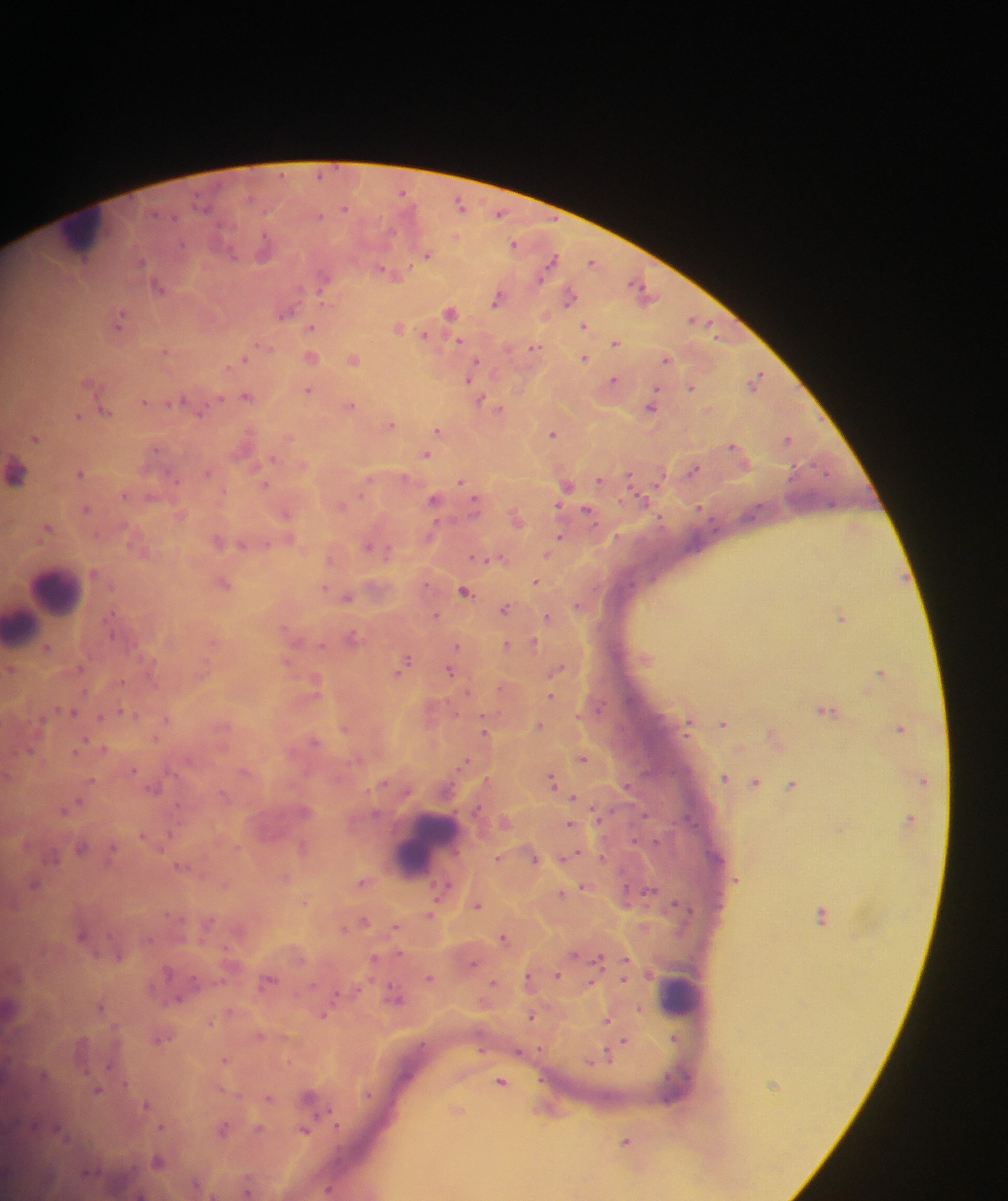 Approximate centers as {x, y} in pixels. Leukocyte locations: {83, 234}, {55, 592}, {20, 626}, {428, 842}, {680, 993}. Plasmodium parasite locations: {402, 192}, {203, 204}, {459, 204}, {344, 208}, {497, 214}, {318, 215}, {180, 244}, {513, 244}, {263, 247}, {427, 255}, {232, 256}, {140, 261}, {549, 261}, {591, 261}, {382, 270}, {323, 277}, {157, 286}, {638, 287}, {568, 297}, {497, 299}, {449, 311}, {285, 313}, {119, 317}, {692, 320}, {584, 325}, {310, 327}, {398, 327}, {423, 335}, {458, 341}, {615, 343}, {536, 347}, {164, 350}, {310, 357}, {584, 358}, {353, 359}, {665, 359}, {239, 361}, {473, 367}, {470, 377}, {756, 379}, {612, 380}, {691, 388}, {307, 390}, {245, 396}, {179, 400}, {143, 401}, {480, 401}, {351, 405}, {651, 406}, {498, 408}, {104, 411}, {76, 415}, {390, 424}, {437, 429}, {551, 434}, {34, 438}, {788, 438}, {732, 446}, {155, 449}, {425, 455}, {271, 458}, {692, 470}, {78, 473}, {206, 473}, {15, 474}, {170, 476}, {630, 477}, {599, 480}, {460, 482}, {264, 484}, {565, 486}, {123, 495}, {641, 499}, {434, 500}, {474, 503}, {832, 505}, {340, 506}, {699, 508}, {85, 509}, {586, 510}, {285, 513}, {46, 528}, {430, 533}, {559, 537}, {217, 542}, {241, 544}, {367, 545}, {386, 552}, {547, 554}, {475, 558}, {535, 582}, {223, 584}, {464, 591}, {346, 597}, {504, 608}, {435, 616}, {841, 616}, {547, 617}, {351, 636}, {212, 641}, {534, 643}, {321, 644}, {506, 644}, {457, 647}, {46, 648}, {403, 662}, {556, 669}, {449, 671}, {879, 672}, {314, 682}, {550, 695}, {825, 710}, {71, 711}, {127, 712}, {99, 717}, {165, 719}, {722, 723}, {539, 725}, {344, 728}, {484, 728}, {900, 728}, {314, 741}, {77, 750}, {29, 751}, {582, 758}, {464, 760}, {243, 772}, {723, 778}, {551, 780}, {754, 783}, {791, 785}, {154, 787}, {223, 795}, {572, 797}, {72, 804}, {62, 810}, {304, 811}, {570, 825}, {142, 835}, {301, 846}, {80, 848}, {111, 850}, {497, 857}, {601, 857}, {534, 859}, {181, 866}, {285, 877}, {361, 882}, {34, 884}, {224, 885}, {582, 886}, {444, 888}, {649, 890}, {560, 893}, {476, 906}, {431, 913}, {821, 914}, {361, 921}, {208, 923}, {395, 928}, {80, 934}, {503, 938}, {398, 953}, {374, 958}, {598, 960}, {472, 962}, {166, 971}, {556, 975}, {429, 978}, {527, 978}, {267, 981}, {492, 983}, {396, 997}, {99, 1006}, {638, 1009}, {323, 1015}, {531, 1017}, {606, 1020}, {210, 1021}, {259, 1036}, {674, 1037}, {158, 1039}, {623, 1041}, {518, 1052}, {605, 1057}, {224, 1059}, {501, 1082}, {97, 1090}, {308, 1097}, {268, 1098}, {145, 1105}, {256, 1128}, {221, 1129}, {304, 1130}, {58, 1131}, {625, 1141}, {157, 1161}, {329, 1190}. Mobile-phone photograph taken through the microscope. One field of view. Sample from Ghana. Image is 1008×1201 pixels. Thick blood smear.